Assess this cell for malaria.
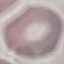
It is uninfected.

Summary:
  - Image type: cell patch, automatically extracted from a larger field of view and resized to 64 × 64 pixels
  - Preparation: thin blood smear
  - Capture: smartphone camera at the microscope eyepiece
  - Stain: Giemsa